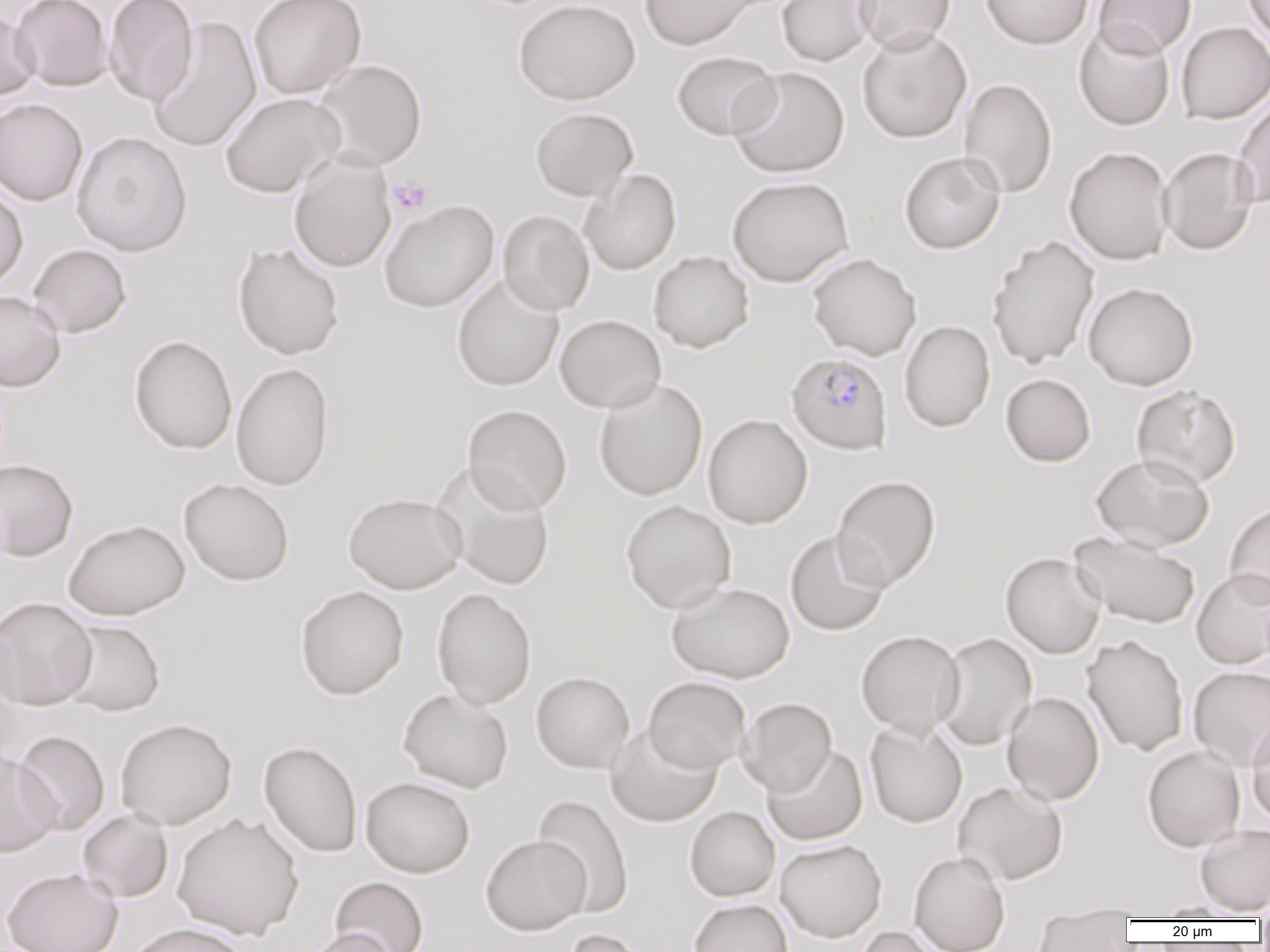
{
  "slide_level_diagnosis": "Plasmodium falciparum",
  "preparation": "thin blood film",
  "magnification": "1000x",
  "modality": "light microscopy",
  "field_of_view": "single",
  "image_size": "1270×952 pixels",
  "platelet_locations": "approximate bounding boxes as named x1/y1/x2/y2 corners in pixels: (x1=388, y1=178, x2=432, y2=215)",
  "uninfected_red_blood_cell_locations": "approximate bounding boxes as named x1/y1/x2/y2 corners in pixels: (x1=12, y1=0, x2=112, y2=92), (x1=103, y1=0, x2=198, y2=106), (x1=247, y1=0, x2=366, y2=99), (x1=513, y1=0, x2=640, y2=105), (x1=639, y1=0, x2=758, y2=50), (x1=776, y1=0, x2=881, y2=66), (x1=855, y1=0, x2=956, y2=54), (x1=979, y1=0, x2=1094, y2=50), (x1=1094, y1=0, x2=1196, y2=57), (x1=1241, y1=0, x2=1270, y2=48), (x1=0, y1=7, x2=41, y2=102), (x1=146, y1=15, x2=262, y2=154), (x1=1073, y1=21, x2=1176, y2=132), (x1=1176, y1=22, x2=1270, y2=124), (x1=856, y1=26, x2=972, y2=144), (x1=671, y1=51, x2=780, y2=141), (x1=311, y1=59, x2=428, y2=171), (x1=728, y1=67, x2=849, y2=178), (x1=958, y1=78, x2=1058, y2=198), (x1=219, y1=92, x2=345, y2=198), (x1=1232, y1=94, x2=1270, y2=208), (x1=0, y1=98, x2=88, y2=206), (x1=530, y1=107, x2=638, y2=201), (x1=71, y1=131, x2=192, y2=257), (x1=1064, y1=147, x2=1173, y2=266), (x1=1158, y1=147, x2=1259, y2=256), (x1=899, y1=152, x2=1006, y2=254), (x1=288, y1=155, x2=397, y2=273), (x1=579, y1=169, x2=682, y2=275), (x1=726, y1=176, x2=854, y2=287), (x1=0, y1=183, x2=28, y2=290), (x1=378, y1=199, x2=499, y2=313), (x1=498, y1=210, x2=595, y2=315), (x1=986, y1=235, x2=1100, y2=370), (x1=232, y1=243, x2=345, y2=360), (x1=27, y1=244, x2=132, y2=338), (x1=648, y1=251, x2=754, y2=353), (x1=807, y1=253, x2=922, y2=361), (x1=451, y1=273, x2=565, y2=392), (x1=1083, y1=282, x2=1199, y2=390), (x1=0, y1=290, x2=66, y2=392), (x1=555, y1=314, x2=666, y2=413), (x1=899, y1=320, x2=995, y2=432), (x1=128, y1=335, x2=237, y2=455), (x1=230, y1=362, x2=334, y2=491), (x1=1000, y1=374, x2=1096, y2=467), (x1=593, y1=379, x2=708, y2=501), (x1=1131, y1=384, x2=1242, y2=488), (x1=462, y1=405, x2=572, y2=515), (x1=702, y1=414, x2=813, y2=529), (x1=1091, y1=454, x2=1215, y2=551), (x1=0, y1=458, x2=79, y2=562), (x1=431, y1=463, x2=556, y2=591), (x1=831, y1=475, x2=941, y2=590), (x1=178, y1=478, x2=295, y2=586), (x1=344, y1=492, x2=468, y2=594), (x1=620, y1=499, x2=737, y2=614), (x1=1224, y1=501, x2=1270, y2=606), (x1=63, y1=519, x2=190, y2=620), (x1=785, y1=531, x2=891, y2=636), (x1=1069, y1=532, x2=1201, y2=629), (x1=1000, y1=552, x2=1106, y2=658), (x1=1191, y1=569, x2=1270, y2=669), (x1=667, y1=582, x2=796, y2=683), (x1=294, y1=585, x2=409, y2=700), (x1=432, y1=588, x2=537, y2=709), (x1=0, y1=597, x2=98, y2=710), (x1=59, y1=619, x2=166, y2=717), (x1=855, y1=630, x2=965, y2=737), (x1=934, y1=633, x2=1037, y2=750), (x1=1082, y1=635, x2=1189, y2=756), (x1=0, y1=637, x2=23, y2=767), (x1=1188, y1=666, x2=1270, y2=770), (x1=531, y1=671, x2=635, y2=773), (x1=643, y1=676, x2=750, y2=773), (x1=398, y1=688, x2=514, y2=793), (x1=1002, y1=691, x2=1105, y2=805), (x1=737, y1=697, x2=837, y2=795), (x1=1246, y1=714, x2=1270, y2=826), (x1=115, y1=718, x2=237, y2=830), (x1=864, y1=718, x2=968, y2=828), (x1=604, y1=725, x2=722, y2=827), (x1=12, y1=730, x2=110, y2=836), (x1=259, y1=741, x2=362, y2=857), (x1=762, y1=745, x2=868, y2=845), (x1=1142, y1=746, x2=1246, y2=852), (x1=0, y1=748, x2=60, y2=858), (x1=361, y1=777, x2=475, y2=878), (x1=952, y1=781, x2=1068, y2=885), (x1=533, y1=794, x2=635, y2=918), (x1=685, y1=806, x2=780, y2=901), (x1=77, y1=808, x2=173, y2=903), (x1=172, y1=813, x2=304, y2=940), (x1=1194, y1=824, x2=1270, y2=915), (x1=480, y1=835, x2=592, y2=935), (x1=775, y1=839, x2=887, y2=941), (x1=908, y1=851, x2=1010, y2=952), (x1=1, y1=866, x2=123, y2=952), (x1=329, y1=876, x2=429, y2=952), (x1=688, y1=899, x2=793, y2=952), (x1=1044, y1=900, x2=1161, y2=917), (x1=1149, y1=900, x2=1255, y2=920), (x1=1031, y1=911, x2=1133, y2=951), (x1=125, y1=922, x2=251, y2=952), (x1=854, y1=926, x2=945, y2=952), (x1=301, y1=928, x2=401, y2=952), (x1=559, y1=928, x2=654, y2=952)",
  "plasmodium_falciparum_infected_red_blood_cell_locations": "approximate bounding boxes as named x1/y1/x2/y2 corners in pixels: (x1=786, y1=352, x2=893, y2=455)"
}